Name the parasite shown.
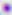

This is Toxoplasma gondii.

Summary:
  - Magnification: 400x
  - Modality: photomicrograph